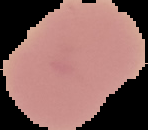
Summary:
  - Image type: cell region segmented out of the field of view; surrounding area masked to black
  - Result: negative for Plasmodium parasites
  - Image size: 148×130 pixels
  - Preparation: thin blood film